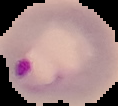
preparation = thin blood smear
image size = 118×106 pixels
malaria status = parasitized
image type = segmented cell region with the area outside set to black